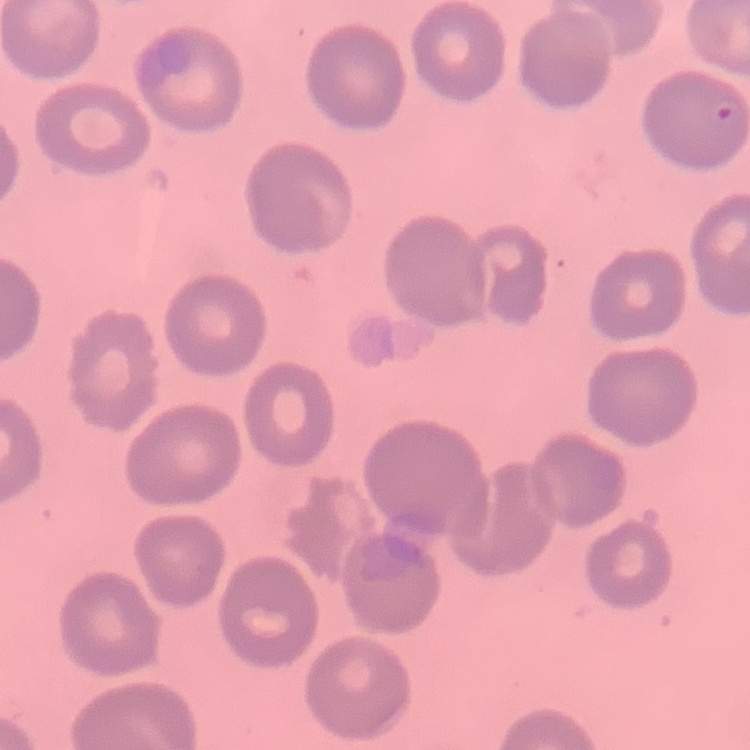
Summary:
  - Red blood cell morphology: no rouleaux formation
  - Preparation: thin blood film
  - Stain: Field's or Giemsa
  - Image type: square crop of a larger photomicrograph